Identify the preparation type.
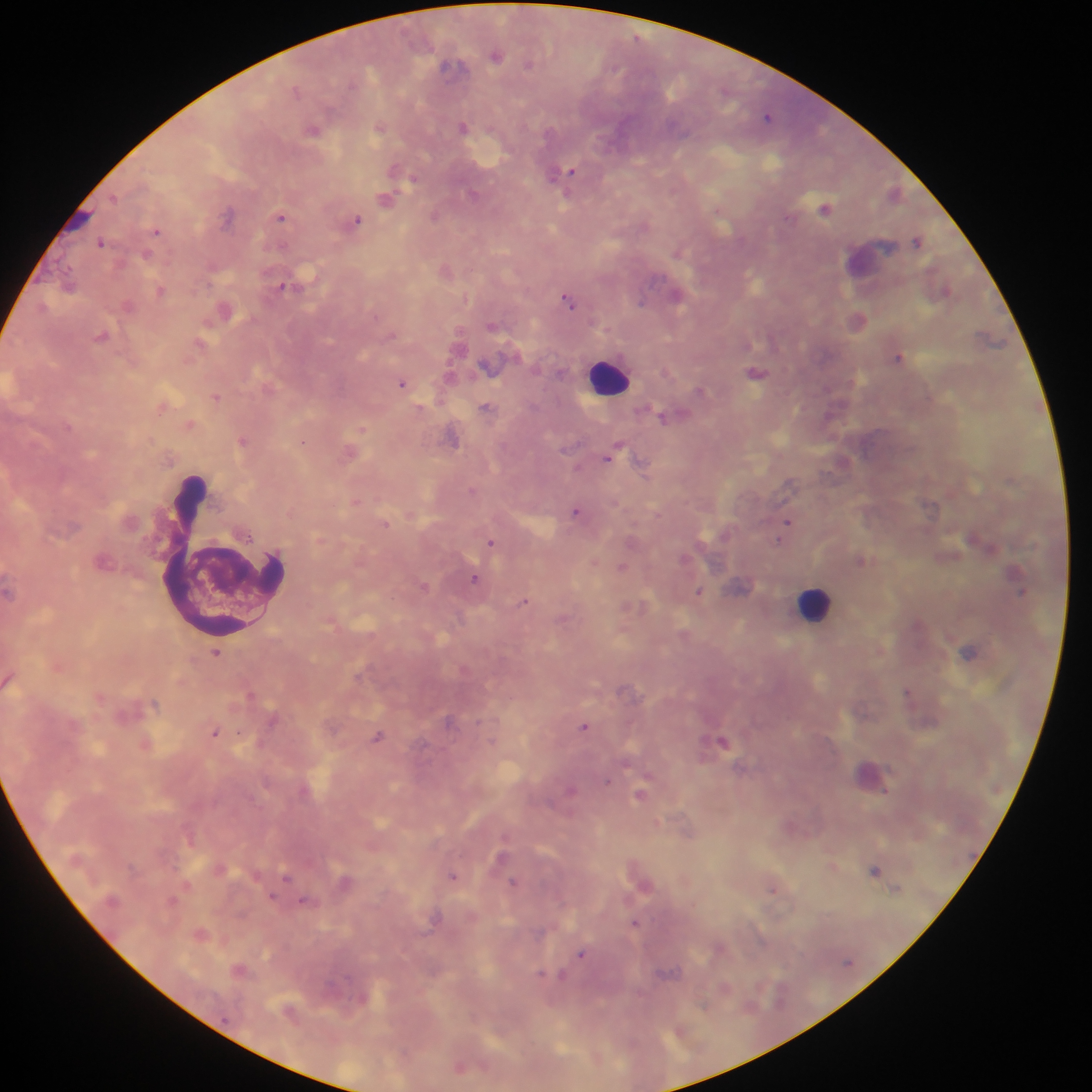

This is a thick smear.

image size = 1092×1092 pixels
field of view = single
leukocyte locations = approximate centers as {x, y} in pixels: {610, 377}, {223, 557}, {815, 603}
malaria parasite locations = approximate centers as {x, y} in pixels: {496, 55}, {529, 64}, {451, 66}, {297, 90}, {767, 116}, {463, 127}, {379, 128}, {312, 130}, {566, 173}, {554, 174}, {415, 179}, {472, 194}, {115, 198}, {385, 199}, {826, 208}, {228, 215}, {434, 215}, {789, 216}, {281, 217}, {356, 220}, {156, 231}, {917, 241}, {101, 243}, {677, 253}, {147, 256}, {69, 283}, {281, 286}, {160, 290}, {947, 290}, {677, 297}, {569, 301}, {641, 302}, {128, 305}, {43, 306}, {858, 320}, {102, 336}, {200, 341}, {898, 358}, {756, 372}, {402, 383}, {700, 391}, {216, 397}, {485, 407}, {829, 414}, {662, 417}, {362, 429}, {453, 438}, {243, 440}, {303, 442}, {570, 445}, {615, 450}, {610, 456}, {641, 464}, {789, 483}, {471, 490}, {576, 510}, {787, 522}, {386, 524}, {490, 541}, {779, 541}, {991, 549}, {861, 559}, {621, 567}, {475, 578}, {423, 585}, {699, 592}, {1021, 592}, {524, 601}, {969, 652}, {216, 653}, {622, 688}, {907, 690}, {251, 695}, {154, 704}, {272, 721}, {584, 726}, {214, 733}, {377, 737}, {722, 741}, {607, 780}, {571, 789}, {640, 795}, {875, 870}, {286, 876}, {453, 876}, {513, 882}, {771, 889}, {273, 897}, {305, 901}, {635, 923}, {581, 954}, {541, 974}, {562, 974}, {459, 1068}
country = Ghana
capture = mobile-phone photograph through a microscope